Identify the parasite.
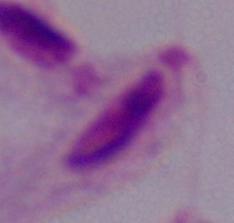
A trichomonad.

1000x magnification. Micrograph.